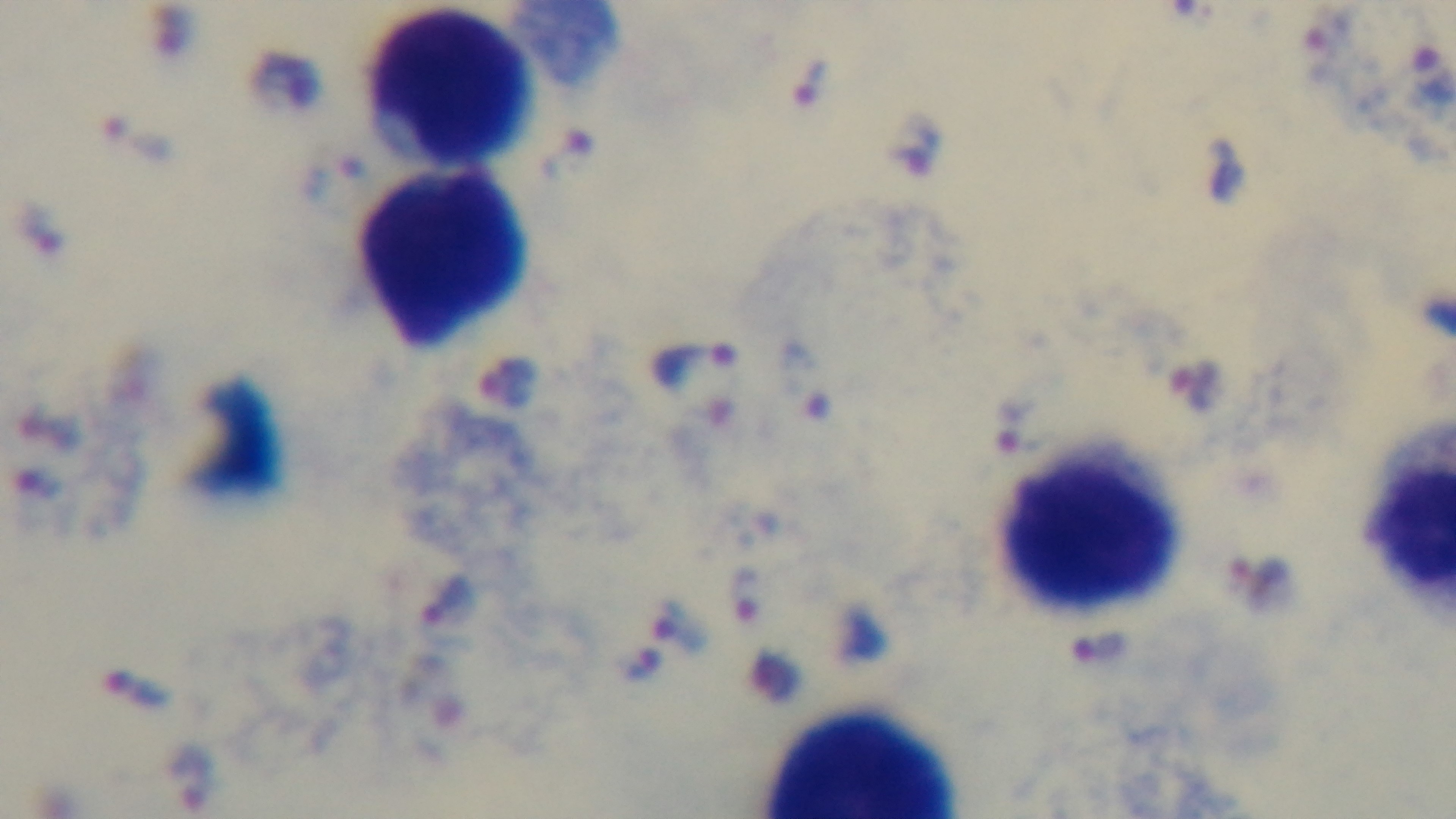 100x oil-immersion objective. Photomicrograph. Preparation: thick blood film. Malaria status: positive. Single field of view. Giemsa stain. Mounted 4K digital camera.